Assess this cell for malaria.
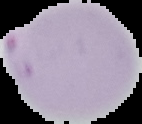

Parasitized.

preparation = thin blood smear
image size = 142×124 pixels
image type = segmented cell region with the area outside set to black